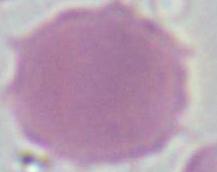

{
  "magnification": "1000x",
  "identification": "erythrocyte",
  "modality": "photomicrograph"
}